Classify this cell by malaria status.
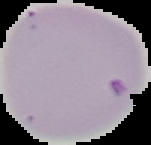
It is parasitized.

{
  "image_size": "151×145 pixels",
  "image_type": "segmented cell region on a black background",
  "preparation": "thin blood smear"
}